Outline platelets.
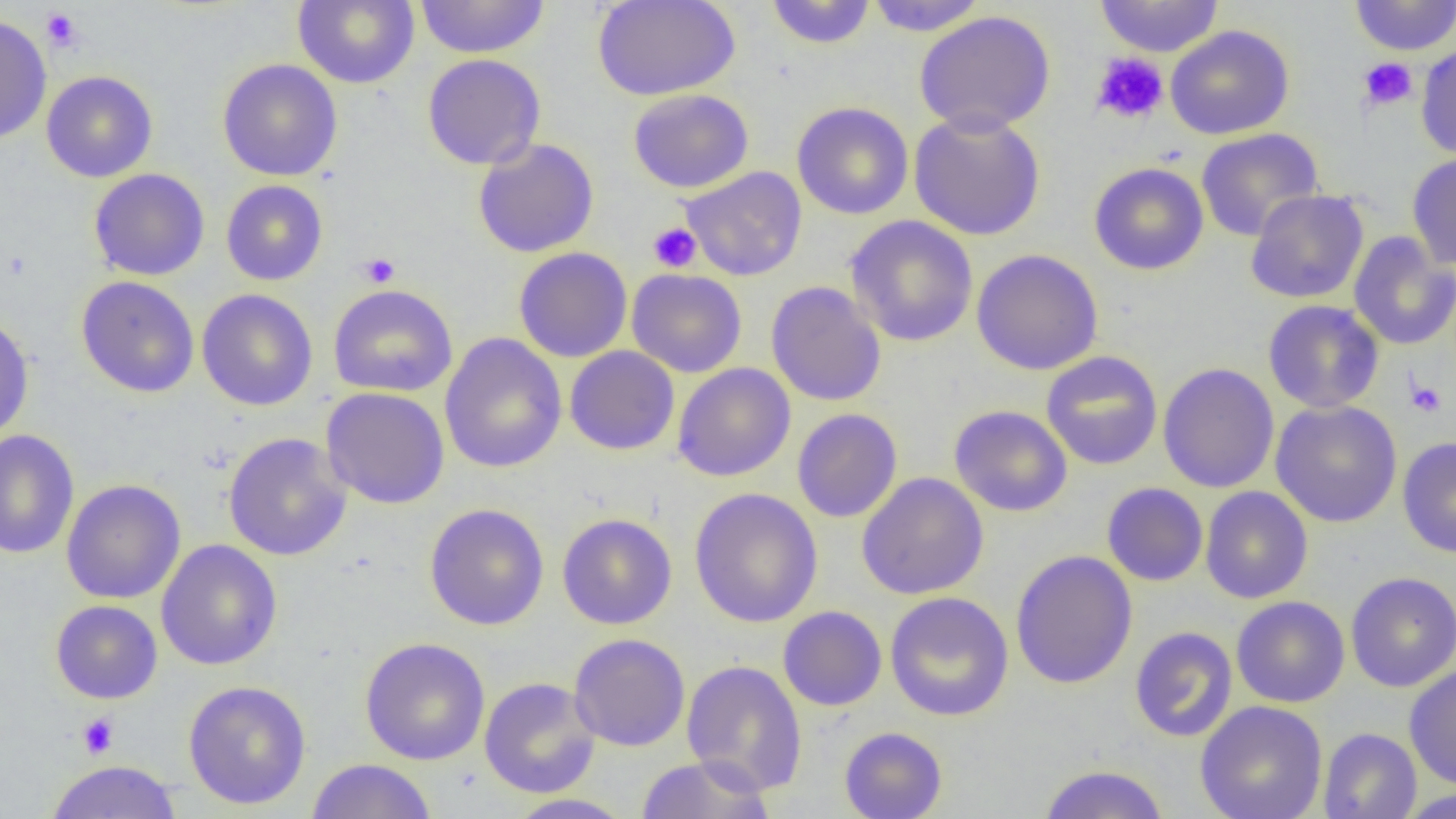

Approximate bounding boxes as [x1, y1, x2, y2] in pixels.
Platelets: [41, 8, 84, 52], [1091, 51, 1168, 125], [1358, 57, 1418, 111], [648, 222, 702, 273], [358, 252, 400, 287], [1405, 378, 1447, 418], [77, 713, 118, 759].

Uninfected red blood cell locations: [293, 0, 419, 89], [414, 0, 551, 59], [592, 0, 741, 100], [863, 0, 989, 36], [1094, 0, 1224, 57], [1349, 0, 1456, 55], [765, 1, 876, 49], [914, 11, 1056, 135], [0, 14, 52, 145], [1165, 24, 1294, 140], [1416, 44, 1456, 159], [422, 53, 546, 170], [217, 58, 343, 181], [41, 70, 158, 183], [628, 89, 754, 193], [791, 102, 913, 220], [908, 110, 1046, 241], [1195, 127, 1324, 242], [472, 138, 599, 258], [1407, 153, 1456, 271], [1089, 162, 1209, 275], [681, 166, 807, 281], [88, 168, 210, 281], [220, 180, 328, 285], [1245, 189, 1369, 304], [845, 215, 978, 347], [1348, 231, 1456, 351], [513, 247, 633, 362], [971, 249, 1104, 375], [627, 268, 747, 378], [76, 276, 199, 397], [766, 281, 887, 407], [328, 284, 458, 397], [196, 289, 318, 411], [1263, 300, 1385, 413], [0, 313, 35, 444], [439, 333, 567, 474], [564, 346, 680, 455], [1041, 351, 1163, 470], [672, 362, 796, 482], [1158, 362, 1279, 493], [320, 387, 450, 509], [1270, 400, 1402, 528], [949, 405, 1073, 517], [792, 408, 903, 523], [0, 430, 79, 559], [223, 432, 353, 561], [1397, 437, 1456, 559], [857, 472, 989, 600], [61, 479, 186, 604], [1101, 482, 1208, 586], [1200, 486, 1313, 604], [689, 487, 823, 628], [424, 503, 549, 630], [557, 513, 676, 629], [156, 540, 283, 670], [1010, 550, 1138, 690], [1345, 571, 1456, 692], [885, 591, 1014, 722], [1231, 596, 1350, 708], [50, 600, 162, 704], [778, 606, 887, 711], [1130, 626, 1238, 742], [568, 633, 690, 752], [360, 637, 490, 765], [682, 659, 807, 795], [1404, 664, 1456, 791], [479, 677, 601, 798], [183, 680, 311, 809], [1196, 700, 1327, 819], [839, 726, 947, 818], [1318, 728, 1422, 819], [635, 755, 776, 818], [306, 759, 437, 818], [45, 760, 182, 818], [1037, 764, 1169, 819], [1397, 788, 1456, 818], [505, 793, 636, 818]. Slide-level diagnosis: no evidence of blood parasites. One field of a larger specimen. Optical microscopy. Captured at 1000x magnification. Image is 1456×819 pixels. Thin blood smear.